Locate every leukocyte (white blood cell).
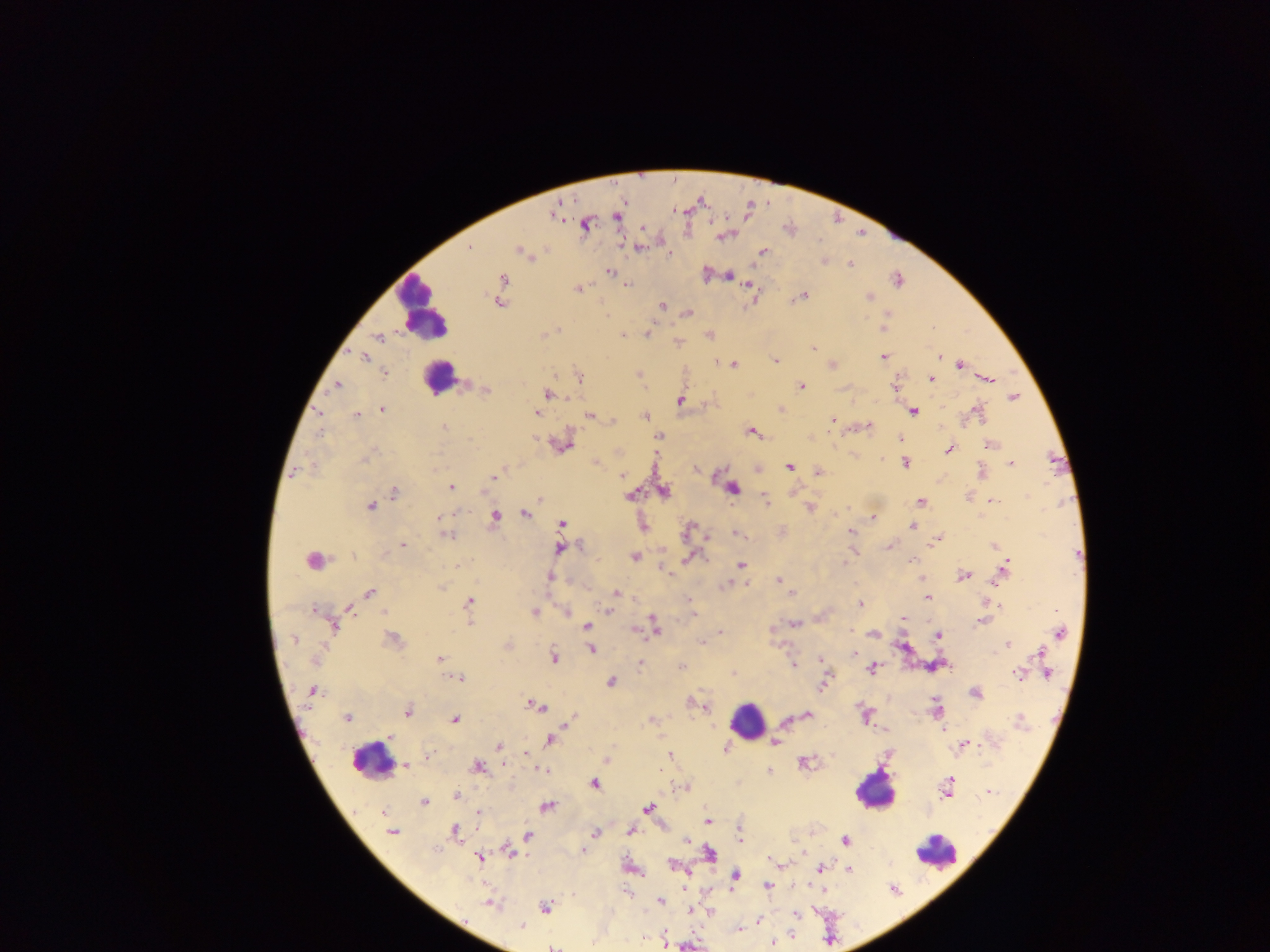
Approximate centers as {x, y} in pixels.
Leukocytes: {422, 309}, {438, 376}, {310, 559}, {748, 721}, {371, 759}, {875, 789}, {935, 850}.

Summary:
  - Plasmodium parasite locations: {554, 214}, {615, 217}, {585, 225}, {644, 227}, {723, 235}, {638, 247}, {470, 248}, {763, 251}, {520, 252}, {669, 253}, {823, 260}, {850, 265}, {609, 272}, {705, 274}, {729, 275}, {898, 280}, {501, 283}, {627, 284}, {748, 284}, {578, 288}, {868, 296}, {801, 297}, {752, 298}, {499, 302}, {662, 305}, {687, 313}, {887, 316}, {883, 326}, {931, 328}, {558, 330}, {647, 333}, {545, 334}, {623, 336}, {709, 336}, {377, 338}, {677, 343}, {813, 349}, {940, 355}, {364, 356}, {884, 357}, {774, 360}, {720, 362}, {733, 364}, {831, 364}, {959, 364}, {384, 373}, {638, 375}, {579, 377}, {930, 379}, {988, 380}, {800, 385}, {895, 385}, {336, 386}, {485, 390}, {548, 394}, {1012, 397}, {679, 399}, {780, 408}, {382, 409}, {912, 410}, {978, 412}, {535, 413}, {590, 415}, {357, 416}, {644, 416}, {832, 419}, {613, 422}, {444, 426}, {867, 426}, {751, 430}, {659, 435}, {534, 439}, {899, 440}, {562, 443}, {989, 444}, {949, 449}, {618, 452}, {368, 455}, {596, 462}, {905, 463}, {1010, 463}, {789, 466}, {697, 469}, {756, 469}, {981, 471}, {818, 472}, {295, 473}, {622, 475}, {495, 476}, {449, 487}, {732, 488}, {663, 491}, {394, 492}, {631, 495}, {763, 498}, {539, 499}, {990, 501}, {921, 502}, {370, 506}, {810, 507}, {525, 513}, {494, 516}, {439, 517}, {872, 518}, {562, 524}, {643, 525}, {913, 525}, {688, 530}, {781, 531}, {851, 531}, {738, 533}, {446, 535}, {708, 538}, {935, 539}, {402, 544}, {889, 545}, {994, 546}, {559, 548}, {853, 551}, {635, 556}, {690, 556}, {911, 561}, {456, 565}, {741, 565}, {1004, 570}, {667, 573}, {963, 575}, {549, 577}, {922, 578}, {779, 580}, {783, 584}, {727, 585}, {369, 592}, {616, 593}, {790, 594}, {926, 596}, {468, 602}, {990, 603}, {860, 604}, {998, 605}, {347, 607}, {314, 609}, {610, 610}, {533, 612}, {566, 612}, {692, 615}, {568, 617}, {902, 618}, {469, 621}, {982, 621}, {794, 623}, {333, 624}, {586, 625}, {653, 625}, {772, 629}, {633, 630}, {720, 632}, {850, 632}, {1058, 632}, {874, 633}, {937, 634}, {717, 637}, {392, 639}, {702, 642}, {507, 645}, {1007, 645}, {902, 647}, {591, 649}, {854, 653}, {1040, 653}, {553, 658}, {314, 659}, {439, 660}, {821, 661}, {639, 663}, {793, 664}, {935, 664}, {681, 666}, {1043, 666}, {873, 668}, {733, 673}, {1019, 673}, {1045, 673}, {458, 678}, {610, 681}, {823, 684}, {312, 691}, {975, 693}, {692, 702}, {701, 704}, {533, 706}, {936, 709}, {407, 711}, {806, 715}, {866, 715}, {347, 717}, {454, 718}, {572, 718}, {652, 720}, {1019, 721}, {885, 729}, {943, 729}, {550, 739}, {774, 742}, {962, 745}, {498, 746}, {725, 748}, {525, 752}, {670, 755}, {607, 758}, {804, 763}, {503, 764}, {406, 765}, {477, 767}, {542, 770}, {768, 772}, {593, 783}, {947, 786}, {685, 787}, {989, 791}, {456, 796}, {423, 802}, {546, 806}, {647, 808}, {478, 813}, {706, 820}, {629, 830}, {392, 831}, {454, 831}, {595, 832}, {739, 833}, {528, 835}, {686, 839}, {845, 840}, {508, 851}, {583, 851}, {709, 854}, {803, 854}, {479, 857}, {769, 859}, {781, 864}, {674, 865}, {631, 867}, {821, 868}, {848, 868}, {734, 875}, {766, 886}, {659, 901}, {490, 903}, {545, 906}, {689, 910}, {710, 912}, {796, 914}, {757, 921}, {521, 926}, {737, 930}, {663, 936}, {664, 942}, {772, 943}, {553, 946}
  - Field of view: single
  - Country: Ghana
  - Image size: 1270×952 pixels
  - Preparation: thick blood film
  - Capture: mobile-phone photograph through a microscope